Report the malaria status of this cell.
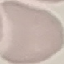

It is uninfected.

stain = Giemsa
preparation = thin blood film
capture = smartphone camera at the microscope eyepiece
image type = automatically extracted cell patch, resized to 64 × 64 pixels